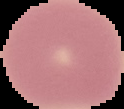

Summary:
  - Image size: 124×109 pixels
  - Image type: segmented cell region on a black background
  - Malaria status: uninfected
  - Preparation: thin blood film